State which cell type is depicted.
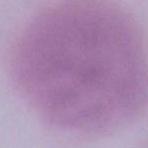
An erythrocyte.

magnification = 1000x
modality = micrograph